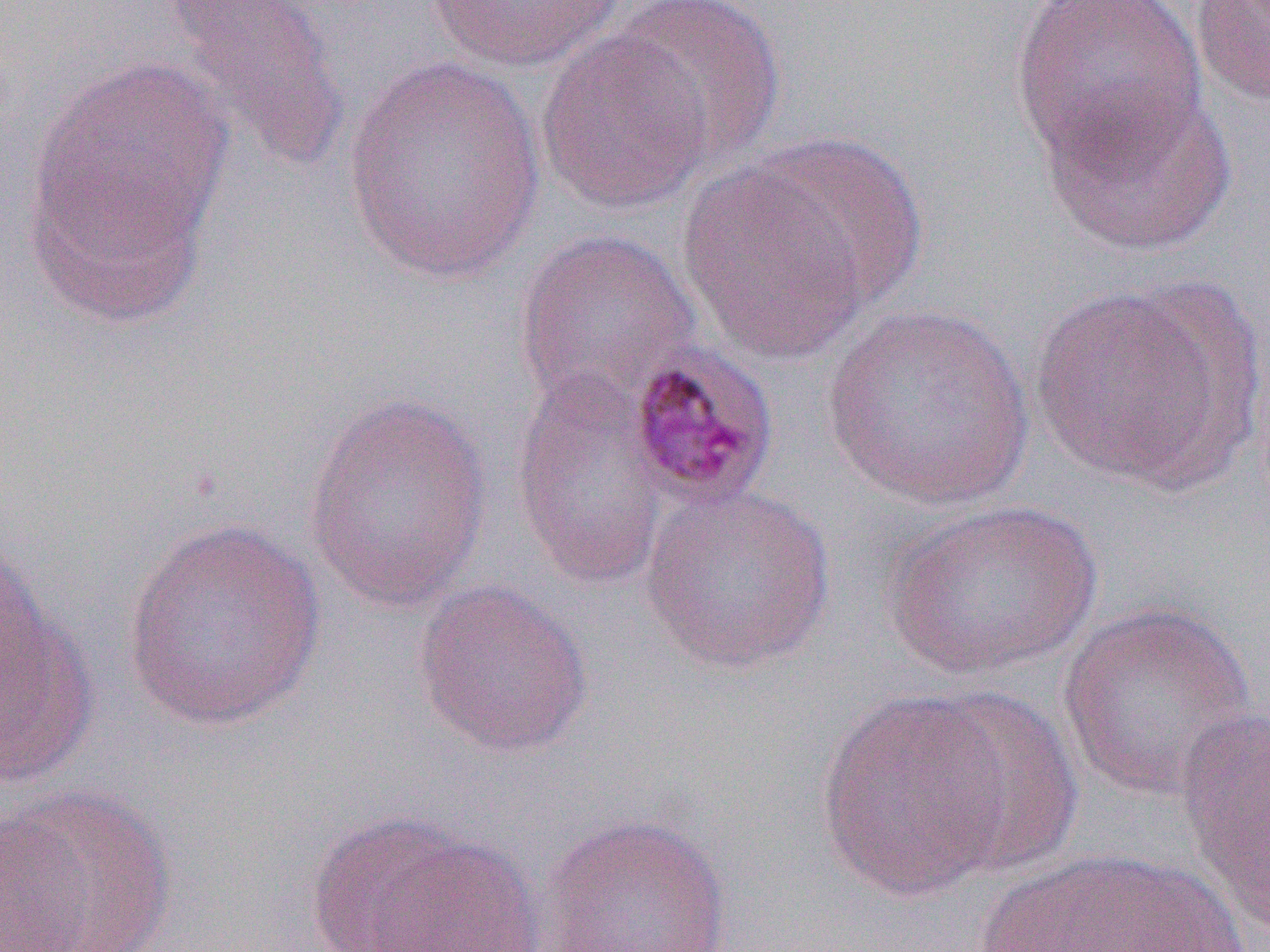

Summary:
  - Coordinate format: approximate bounding boxes as named x1/y1/x2/y2 corners in pixels
  - Plasmodium malariae-infected red blood cell locations: (x1=624, y1=340, x2=781, y2=511)
  - Uninfected red blood cell locations: (x1=158, y1=0, x2=353, y2=176), (x1=424, y1=0, x2=628, y2=72), (x1=610, y1=0, x2=786, y2=168), (x1=1009, y1=0, x2=1208, y2=170), (x1=1189, y1=0, x2=1270, y2=107), (x1=535, y1=26, x2=716, y2=216), (x1=24, y1=52, x2=237, y2=308), (x1=344, y1=55, x2=546, y2=285), (x1=1037, y1=83, x2=1237, y2=257), (x1=746, y1=133, x2=929, y2=309), (x1=677, y1=160, x2=875, y2=365), (x1=513, y1=226, x2=702, y2=416), (x1=1027, y1=282, x2=1250, y2=491), (x1=821, y1=304, x2=1036, y2=511), (x1=509, y1=367, x2=671, y2=592), (x1=302, y1=392, x2=494, y2=614), (x1=639, y1=483, x2=837, y2=674), (x1=881, y1=498, x2=1101, y2=682), (x1=119, y1=517, x2=329, y2=732), (x1=412, y1=579, x2=594, y2=759), (x1=0, y1=583, x2=99, y2=790), (x1=1056, y1=600, x2=1259, y2=802), (x1=921, y1=687, x2=1083, y2=876), (x1=816, y1=688, x2=1019, y2=902), (x1=1175, y1=708, x2=1270, y2=938), (x1=0, y1=783, x2=177, y2=952), (x1=303, y1=811, x2=545, y2=952), (x1=535, y1=813, x2=733, y2=952), (x1=968, y1=846, x2=1253, y2=952)
  - Slide-level diagnosis: Plasmodium malariae
  - Modality: optical microscopy
  - Field of view: one of a larger specimen
  - Image size: 1270×952 pixels
  - Magnification: 1000x
  - Preparation: thin blood smear